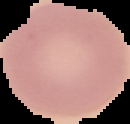
image type = cell region segmented out of the field of view; surrounding area masked to black
malaria status = uninfected
preparation = thin blood film
image size = 130×124 pixels